Assess this cell for malaria.
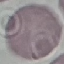

It is uninfected.

{
  "stain": "Giemsa",
  "preparation": "thin blood smear",
  "capture": "smartphone camera at the microscope eyepiece",
  "image_type": "automatically extracted cell patch, resized to 64 × 64 pixels"
}